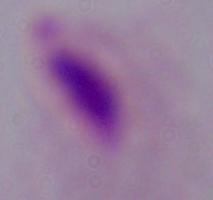

Summary:
  - Magnification: 1000x
  - Identification: trichomonad
  - Modality: micrograph